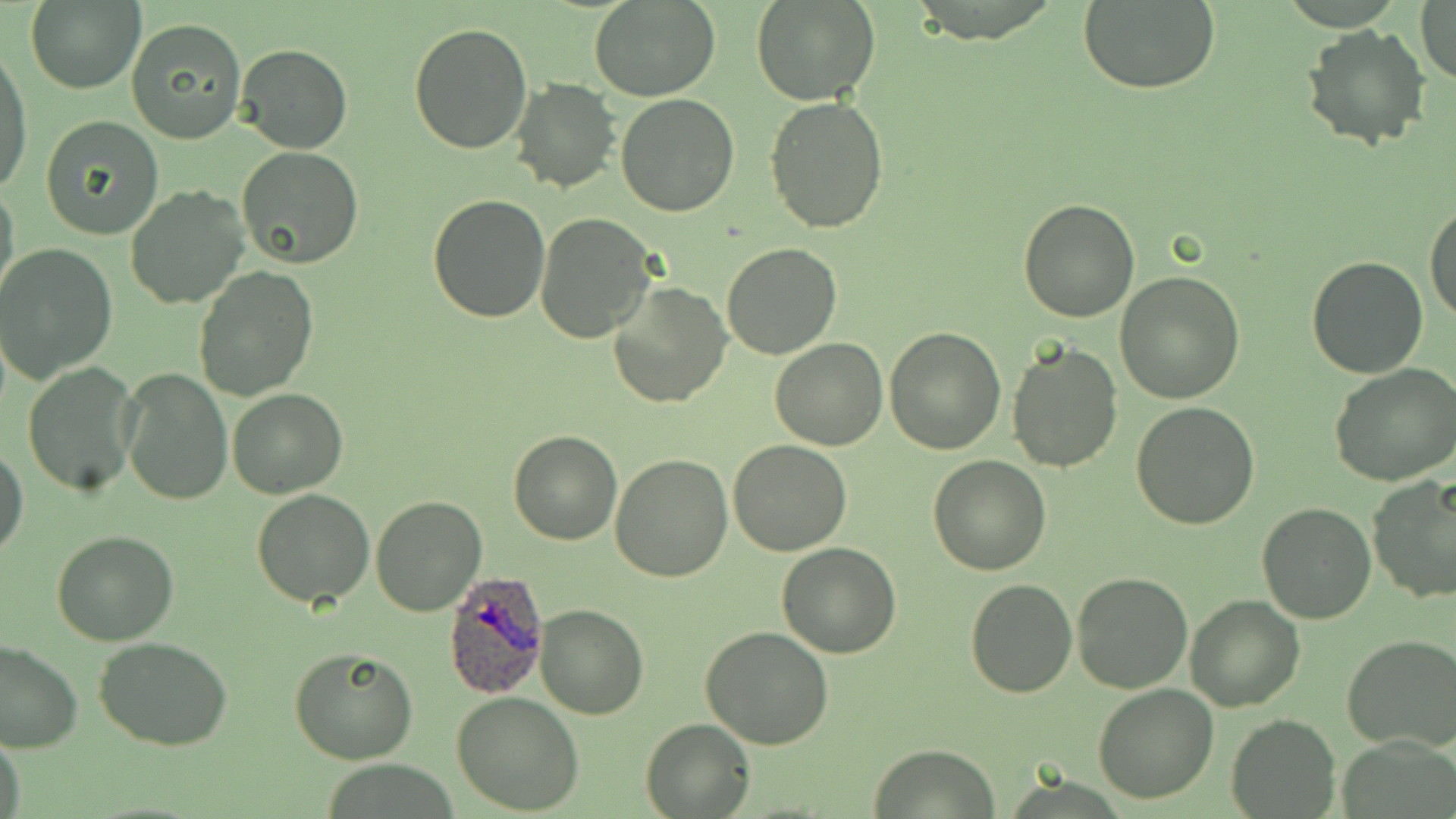
Approximate bounding boxes as [x1, y1, x2, y2] in pixels. Uninfected red blood cell locations: [24, 0, 146, 95], [589, 0, 720, 101], [751, 0, 880, 106], [1077, 3, 1220, 93], [1416, 3, 1456, 85], [126, 18, 248, 144], [407, 22, 532, 155], [1301, 24, 1432, 152], [235, 43, 352, 155], [0, 45, 33, 198], [510, 77, 621, 194], [615, 93, 740, 217], [765, 96, 889, 232], [39, 115, 164, 240], [237, 145, 364, 268], [0, 180, 20, 308], [124, 185, 250, 312], [426, 194, 551, 323], [1017, 198, 1142, 321], [1425, 204, 1456, 326], [535, 212, 658, 343], [721, 242, 842, 359], [0, 244, 118, 382], [1305, 255, 1429, 379], [192, 266, 319, 401], [1115, 272, 1246, 405], [608, 280, 730, 408], [884, 326, 1006, 455], [771, 340, 889, 451], [1006, 340, 1124, 472], [1331, 360, 1456, 485], [22, 362, 140, 499], [119, 367, 233, 506], [225, 388, 347, 498], [1130, 402, 1260, 531], [508, 429, 624, 546], [729, 438, 852, 555], [0, 444, 27, 561], [610, 454, 732, 582], [929, 454, 1052, 575], [1367, 474, 1456, 607], [251, 488, 377, 608], [371, 496, 488, 617], [1256, 501, 1377, 624], [51, 528, 180, 645], [776, 543, 902, 658], [1071, 570, 1195, 695], [966, 578, 1077, 697], [1185, 595, 1304, 712], [534, 602, 649, 719], [701, 626, 834, 749], [1343, 634, 1456, 750], [93, 635, 235, 751], [0, 640, 81, 754], [288, 648, 419, 765], [1093, 685, 1218, 803], [452, 690, 585, 813], [1226, 713, 1339, 818], [641, 717, 755, 818], [0, 735, 25, 819], [871, 743, 1001, 818]. Plasmodium ovale-infected red blood cell locations: [443, 572, 549, 697]. Slide-level diagnosis: Plasmodium ovale. Light microscopy. Image is 1456×819 pixels. One field of a larger specimen. May-Grünwald-Giemsa stain. Captured at 1000x magnification. Thin blood film.